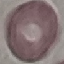
Result: no malaria parasites seen. Cell patch, automatically extracted from a larger field of view and resized to 64 × 64 pixels. Acquired by smartphone through the microscope eyepiece. Thin blood smear. Giemsa stain.